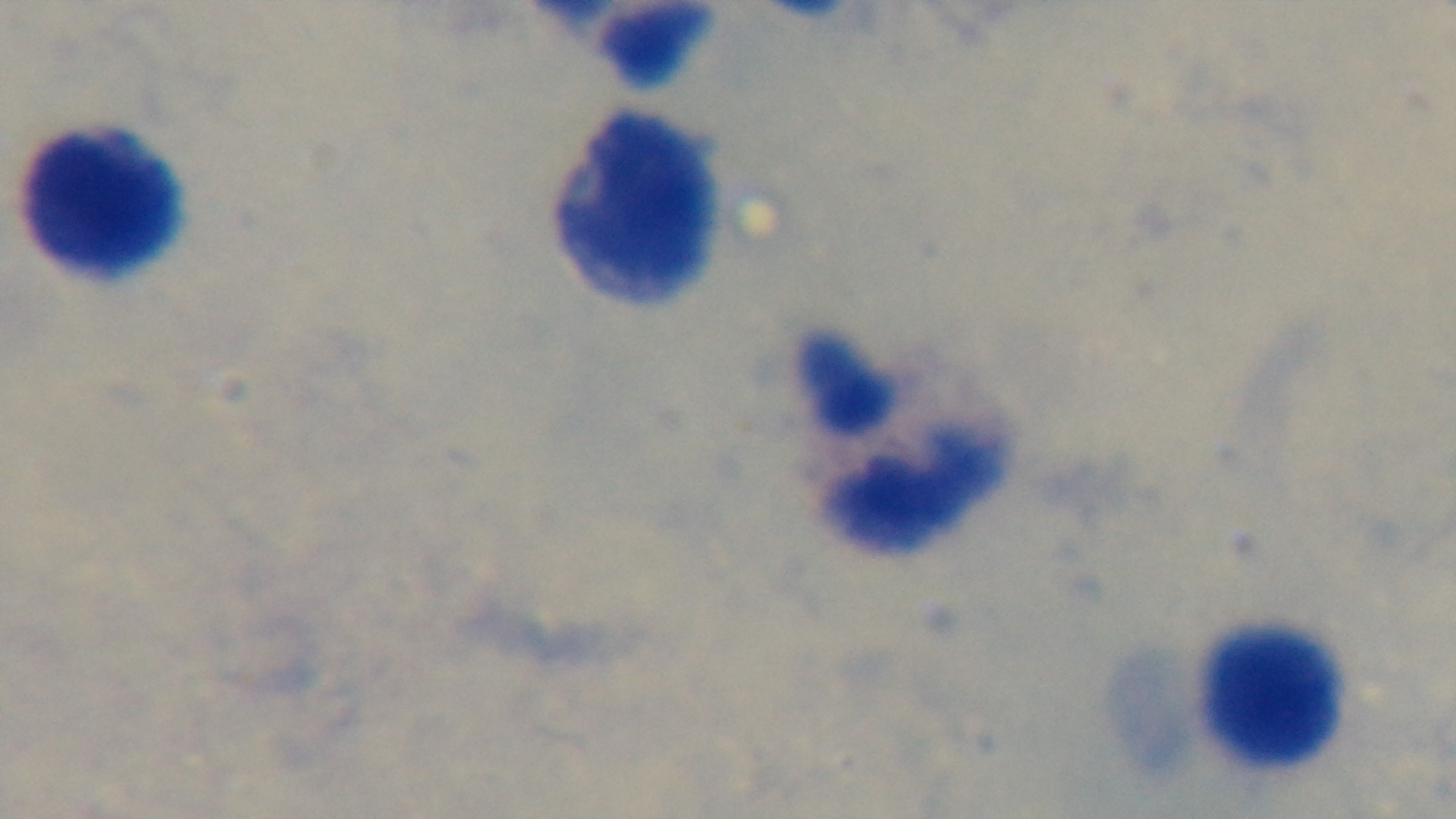

Summary:
  - Modality: light microscopy
  - Preparation: thick
  - Capture: mounted 4K digital camera
  - Objective: 100x oil immersion
  - Stain: Giemsa
  - Field of view: one from the slide
  - Malaria status: uninfected